State the blood parasite species.
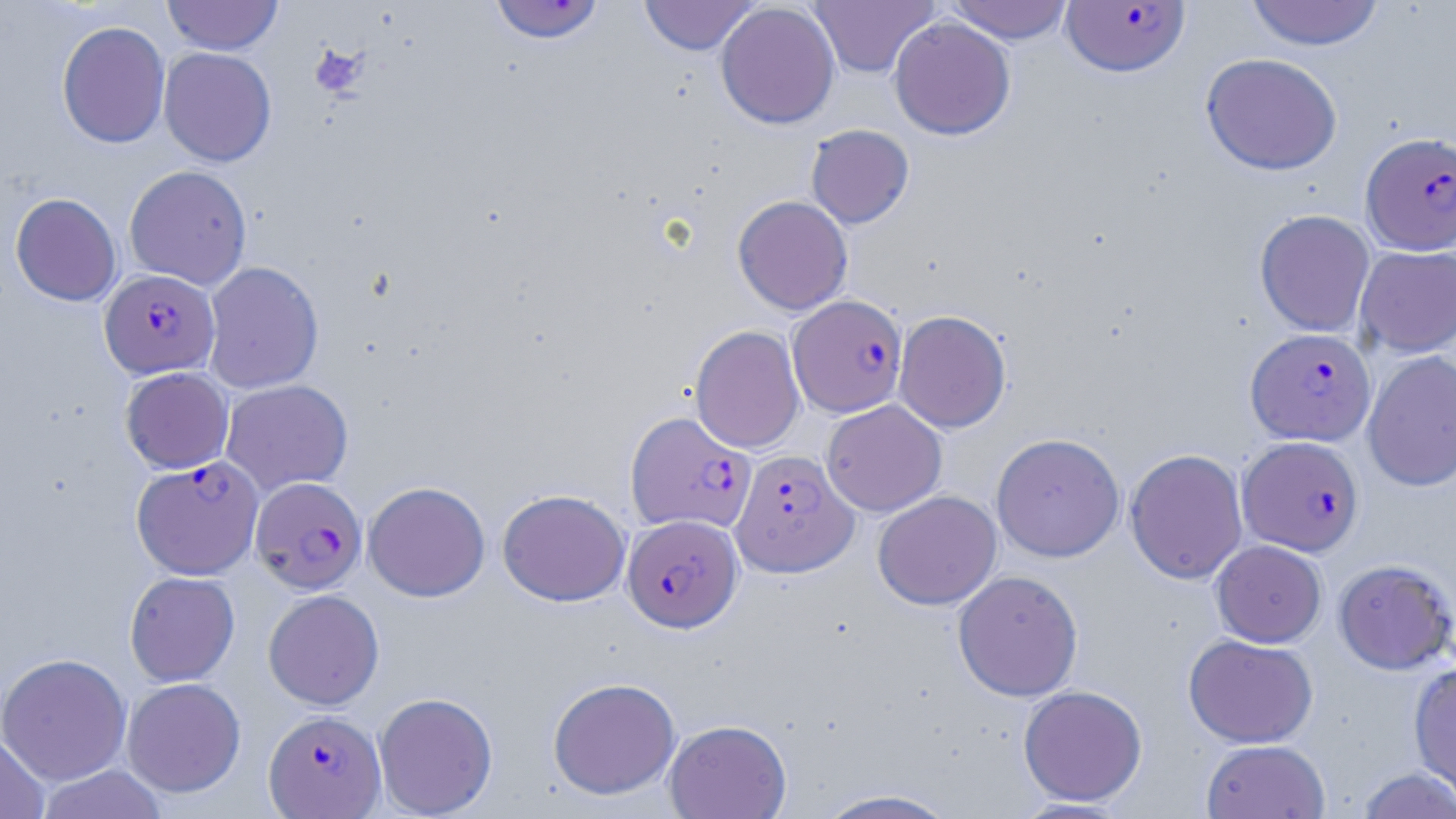
Plasmodium falciparum.

magnification = 1000x
field of view = single
Plasmodium falciparum-infected red blood cell locations = approximate bounding boxes as (x1,y1)-(x2,y2) corner pairs in pixels: (488,0)-(606,45), (1060,1)-(1190,77), (1361,132)-(1456,255), (99,269)-(220,379), (788,295)-(907,418), (1245,328)-(1375,446), (625,410)-(756,535), (1237,436)-(1364,556), (731,449)-(857,577), (131,457)-(263,579), (250,477)-(367,594), (622,514)-(742,632), (264,710)-(386,817)
image size = 1456×819 pixels
stain = May-Grünwald-Giemsa
preparation = thin blood smear
modality = optical microscopy
uninfected red blood cell locations = approximate bounding boxes as (x1,y1)-(x2,y2) corner pairs in pixels: (162,0)-(284,55), (639,0)-(760,55), (806,0)-(939,78), (945,0)-(1076,44), (1244,0)-(1385,50), (715,2)-(840,129), (888,16)-(1016,140), (56,21)-(170,149), (158,47)-(277,167), (1200,52)-(1342,175), (805,124)-(914,229), (124,165)-(252,289), (10,193)-(121,306), (732,195)-(853,315), (1254,209)-(1376,337), (1355,246)-(1456,357), (202,261)-(324,393), (893,310)-(1012,433), (690,325)-(805,454), (1362,351)-(1456,491), (120,367)-(234,473), (221,379)-(353,495), (822,399)-(947,516), (991,433)-(1125,562), (1124,448)-(1248,584), (363,481)-(490,601), (497,489)-(630,607), (872,490)-(1002,610), (1211,540)-(1327,647), (1333,559)-(1455,674), (952,569)-(1083,701), (124,571)-(240,686), (263,589)-(384,710), (1184,634)-(1318,748), (0,653)-(131,785), (1408,661)-(1456,802), (122,677)-(246,797), (547,677)-(681,800), (1018,685)-(1147,806), (374,691)-(498,817), (664,719)-(792,819), (0,731)-(50,819), (1201,740)-(1330,819), (36,764)-(168,819), (1356,766)-(1456,819), (812,788)-(963,818), (1011,798)-(1133,818)